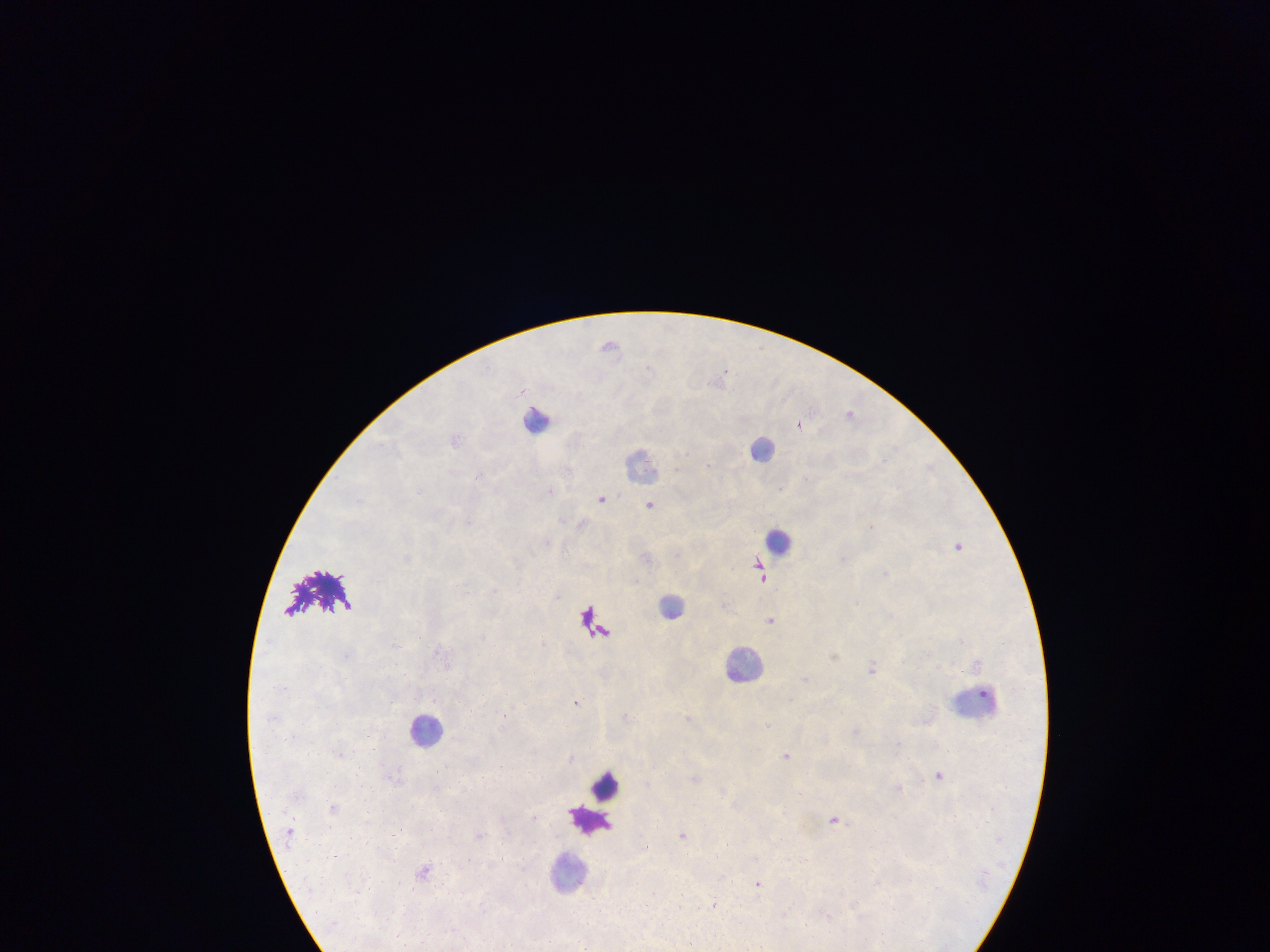

malaria parasite locations = approximate centers as (x, y) in pixels: (610, 345), (721, 377), (851, 413), (799, 423), (602, 498), (650, 504), (871, 527), (958, 544), (845, 558), (760, 567), (886, 573), (763, 575), (772, 619), (872, 669), (806, 678), (577, 702), (505, 715), (689, 717), (767, 724), (857, 732), (787, 755), (940, 773), (695, 778), (899, 788), (534, 816), (836, 819), (480, 835), (683, 835), (726, 845), (423, 869), (758, 884), (716, 903), (679, 907), (828, 915)
image size = 1270×952 pixels
capture = mobile-phone photograph through a microscope
leukocyte locations = approximate centers as (x, y) in pixels: (536, 418), (763, 448), (642, 464), (780, 541), (323, 594), (671, 606), (592, 623), (743, 665), (975, 702), (425, 729), (607, 786), (591, 819), (568, 872)
field of view = single
preparation = thick blood film
country = Ghana